Assess the morphology of the erythrocytes.
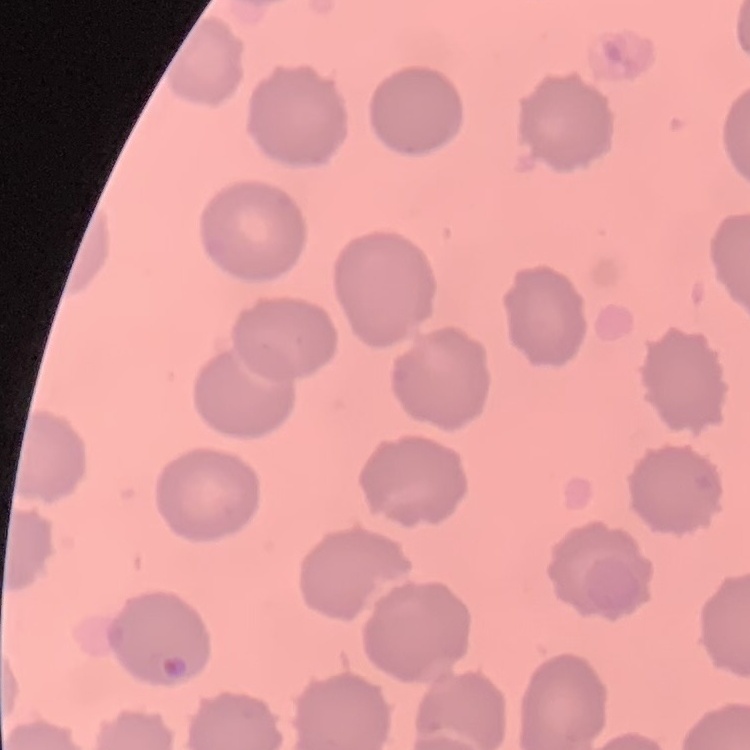
No rouleaux formation.

Stained with either Field's or Giemsa. Square crop of a larger photomicrograph. Thin blood film.